Outline each blood parasite and name the species.
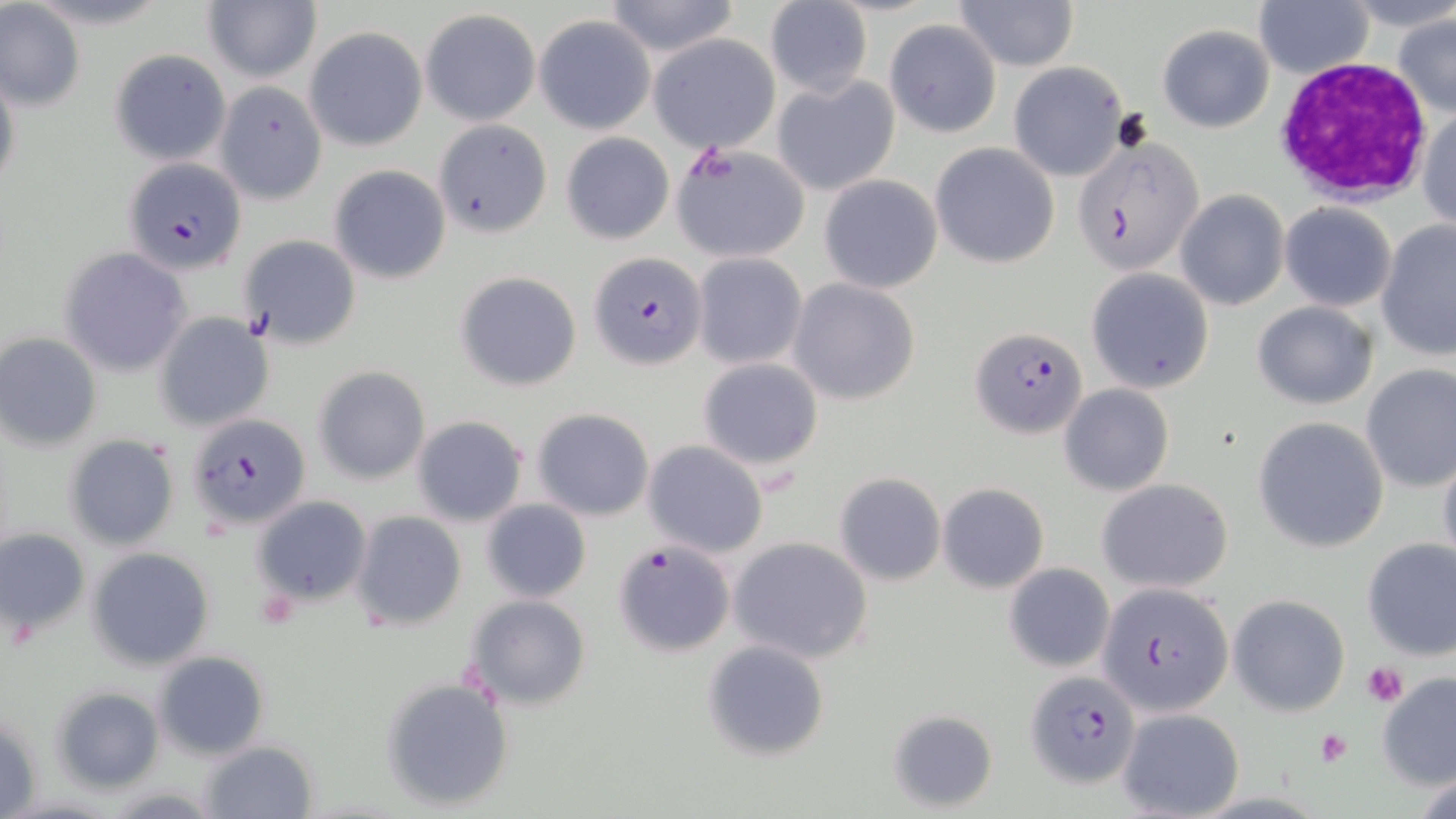
Approximate bounding boxes as (x1,y1)-(x2,y2) corner pairs in pixels.
Plasmodium falciparum-infected red blood cells: (1073,136)-(1205,276), (122,158)-(246,274), (588,253)-(706,371), (969,325)-(1087,438), (185,413)-(311,531), (612,539)-(734,655), (1100,582)-(1234,718), (1025,669)-(1141,788).
No Plasmodium ovale, Plasmodium malariae, Plasmodium vivax, Babesia divergens, or Trypanosoma brucei observed.

Platelet locations: (1113,107)-(1153,154), (1363,661)-(1409,708), (1314,729)-(1352,767). White blood cell locations: (1272,59)-(1431,202). Uninfected red blood cell locations: (203,0)-(320,85), (602,0)-(743,56), (953,0)-(1077,70), (1252,0)-(1374,79), (1340,0)-(1456,34), (763,2)-(872,97), (1,4)-(83,111), (421,9)-(540,125), (1392,12)-(1455,119), (535,15)-(655,133), (883,19)-(1002,137), (1158,24)-(1274,132), (305,26)-(427,151), (651,34)-(781,153), (109,48)-(232,167), (1008,61)-(1128,180), (0,67)-(20,202), (771,75)-(900,197), (215,81)-(329,204), (1417,105)-(1455,232), (434,119)-(553,237), (561,133)-(675,245), (669,143)-(810,263), (930,143)-(1059,268), (328,166)-(451,284), (818,174)-(943,294), (1175,190)-(1288,311), (1280,202)-(1396,311), (1376,221)-(1456,359), (240,235)-(362,349), (61,246)-(191,376), (692,253)-(807,370), (1085,268)-(1213,392), (455,271)-(582,391), (790,278)-(920,405), (1253,301)-(1378,410), (154,313)-(275,430), (0,332)-(102,448), (697,358)-(824,469), (1360,363)-(1456,492), (314,367)-(430,483), (1060,384)-(1173,496), (533,408)-(654,519), (411,415)-(528,527), (1253,416)-(1389,552), (63,433)-(180,551), (642,441)-(768,556), (1435,445)-(1456,576), (833,472)-(945,587), (1098,478)-(1234,594), (936,482)-(1050,594), (255,496)-(372,604), (481,500)-(591,603), (352,511)-(467,630), (0,526)-(89,644), (728,536)-(875,665), (1361,538)-(1456,660), (88,547)-(215,668), (1004,563)-(1115,669), (1230,594)-(1349,717), (465,596)-(592,710), (703,641)-(830,763), (154,651)-(270,759), (1376,671)-(1455,791), (379,678)-(515,811), (50,686)-(164,795), (1116,707)-(1244,819), (886,708)-(998,813), (2,711)-(41,817), (198,739)-(319,818), (102,785)-(225,816). Slide-level diagnosis: Plasmodium falciparum. Image is 1456×819 pixels. One field of a larger specimen. Thin blood film. Light microscopy. May-Grünwald-Giemsa-stained preparation. Captured at 1000x magnification.